Point out each Plasmodium parasite.
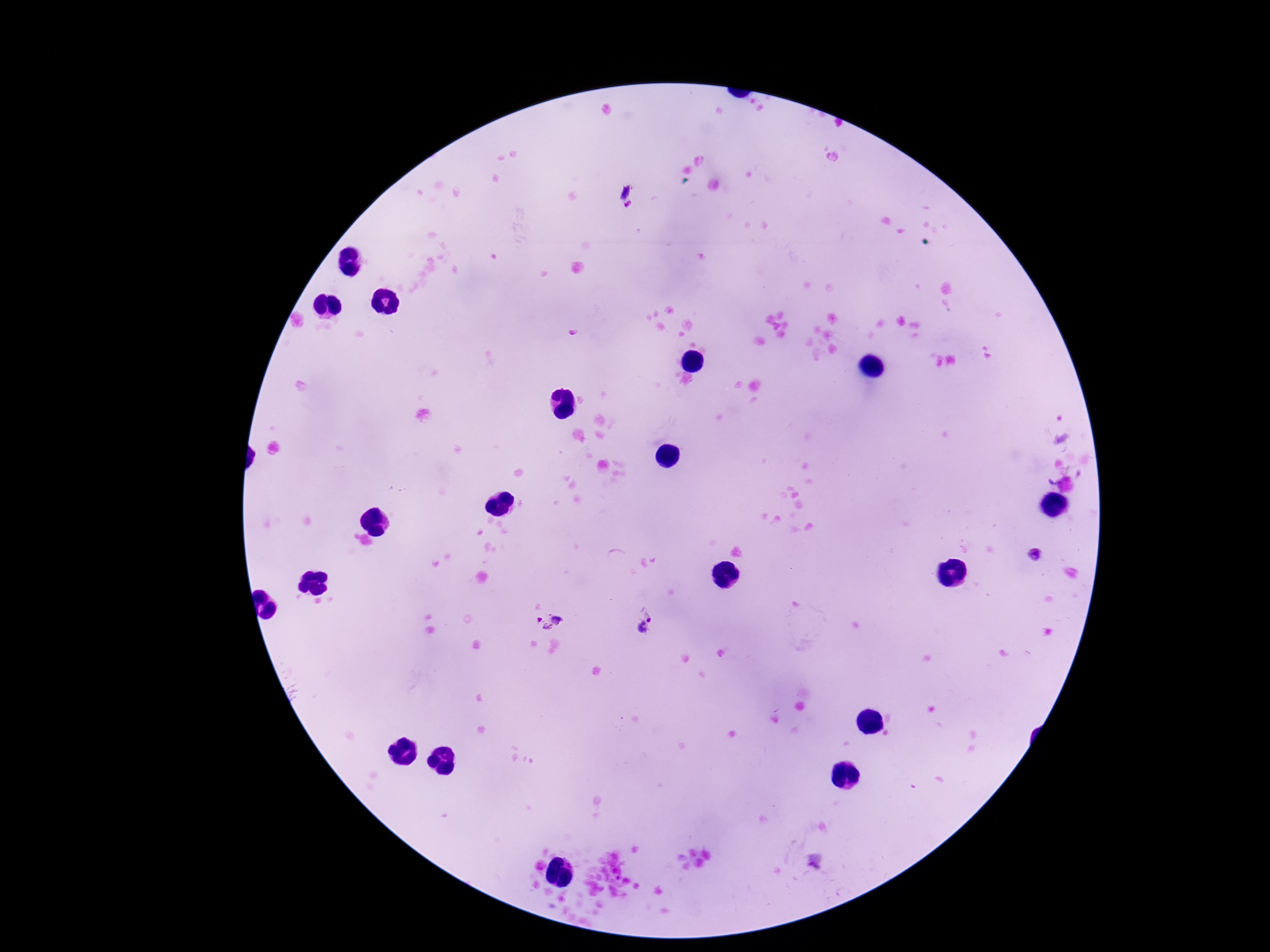

Approximate centers as (x, y) in pixels.
Plasmodium parasites: (625, 192), (629, 205), (1035, 557), (550, 621), (648, 623).

Thick peripheral-blood smear. Giemsa stain. 100x magnification. Patient malaria status: infected. Image is 1270×952 pixels. One field from this slide. Smartphone photograph taken through the microscope eyepiece.